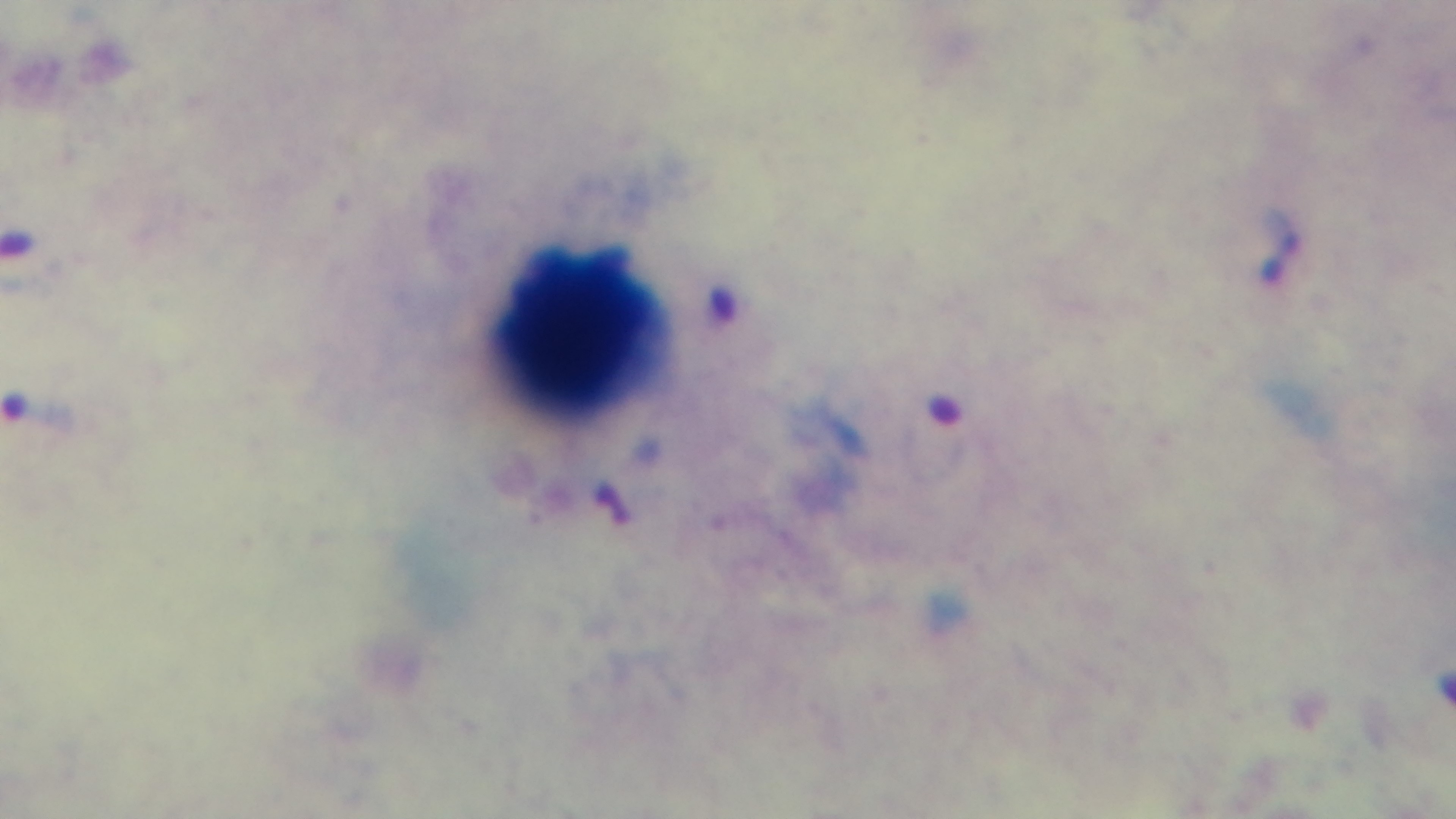 Preparation: thick. Malaria status: positive. Giemsa stain. Photomicrograph. 100x oil-immersion objective. Mounted 4K digital camera. One field from the slide.